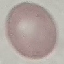 Malaria status: uninfected. Cell patch, automatically extracted from a larger field of view and resized to 64 × 64 pixels. Giemsa stain. Thin blood film. Acquired by smartphone through the microscope eyepiece.